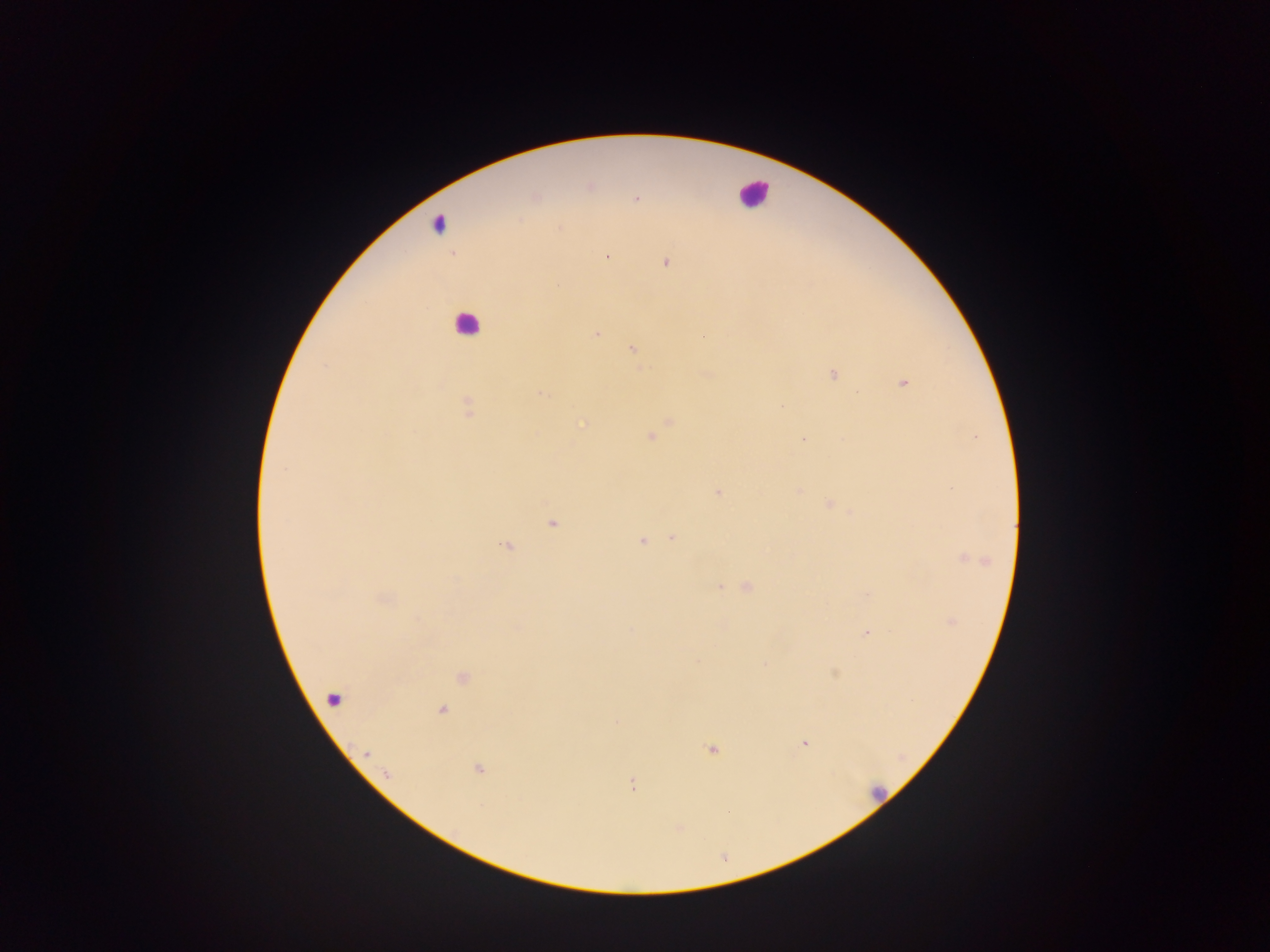
Approximate centers as (x, y) in pixels.
Summary:
  - Malaria parasite locations: (589, 188), (536, 197), (636, 199), (559, 228), (606, 256), (666, 263), (596, 333), (632, 349), (326, 366), (833, 374), (904, 383), (540, 394), (781, 405), (469, 409), (670, 421), (582, 425), (651, 437), (804, 439), (717, 493), (828, 504), (553, 523), (672, 538), (641, 541), (507, 547), (970, 558), (719, 587), (747, 587), (952, 622), (866, 634), (698, 660), (765, 665), (463, 678), (334, 698), (441, 710), (805, 743), (711, 749), (479, 770), (633, 785), (728, 811)
  - Leukocyte locations: (752, 192), (437, 223), (466, 324), (876, 793)
  - Capture: mobile-phone photograph through a microscope
  - Image size: 1270×952 pixels
  - Field of view: single
  - Preparation: thick blood smear
  - Country: Ghana